Locate and identify every blood parasite.
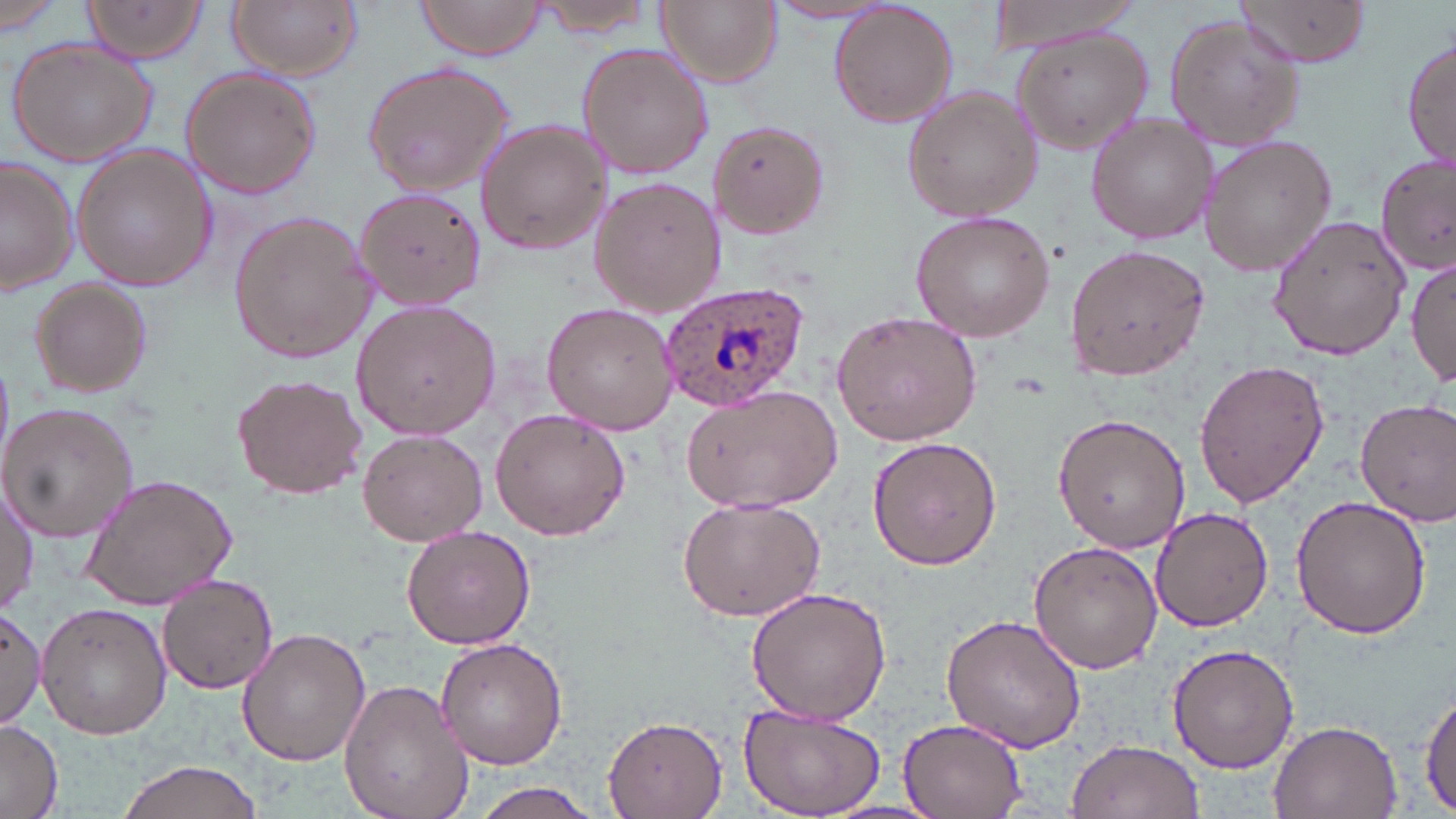

Approximate bounding boxes as [x1, y1, x2, y2] in pixels.
Plasmodium ovale-infected red blood cells: [657, 282, 811, 409].
No Plasmodium falciparum, Plasmodium malariae, Plasmodium vivax, Babesia divergens, or Trypanosoma brucei observed.

slide-level diagnosis = Plasmodium ovale
magnification = 1000x
field of view = one of a larger specimen
stain = May-Grünwald-Giemsa
preparation = thin blood smear
uninfected red blood cell locations = approximate bounding boxes as [x1, y1, x2, y2] in pixels: [80, 0, 211, 65], [226, 0, 362, 80], [529, 0, 659, 39], [658, 0, 781, 88], [985, 0, 1154, 54], [1232, 0, 1374, 70], [0, 1, 70, 33], [413, 1, 549, 63], [828, 1, 960, 130], [766, 3, 900, 25], [1162, 14, 1306, 152], [1010, 28, 1156, 155], [1401, 32, 1454, 172], [7, 37, 158, 168], [577, 42, 712, 180], [359, 59, 519, 195], [178, 66, 321, 199], [901, 85, 1041, 224], [1085, 111, 1218, 245], [707, 116, 829, 240], [472, 119, 610, 252], [1196, 133, 1336, 278], [71, 146, 217, 292], [1377, 151, 1454, 276], [0, 158, 76, 295], [588, 177, 728, 317], [354, 185, 487, 310], [227, 210, 377, 362], [908, 210, 1056, 341], [1268, 212, 1412, 360], [1063, 244, 1212, 381], [1409, 256, 1456, 387], [28, 279, 154, 400], [350, 299, 500, 438], [542, 302, 677, 434], [830, 311, 982, 446], [1193, 357, 1329, 509], [232, 373, 367, 500], [677, 383, 844, 514], [1355, 396, 1456, 528], [0, 402, 138, 541], [489, 407, 631, 541], [1052, 413, 1189, 552], [357, 428, 488, 545], [867, 436, 1001, 572], [76, 474, 239, 610], [0, 482, 38, 613], [1290, 493, 1431, 639], [676, 494, 827, 622], [1150, 505, 1276, 631], [400, 524, 535, 649], [1029, 540, 1164, 675], [157, 574, 280, 694], [741, 586, 892, 725], [36, 602, 171, 739], [1, 605, 48, 731], [939, 614, 1087, 753], [235, 626, 371, 766], [436, 637, 567, 770], [1165, 642, 1300, 773], [339, 677, 476, 819], [1416, 689, 1455, 815], [734, 703, 885, 819], [898, 716, 1029, 819], [0, 717, 62, 819], [603, 717, 727, 817], [1268, 718, 1403, 819], [1066, 738, 1203, 819], [114, 758, 269, 819], [466, 783, 607, 818]
modality = optical microscopy
image size = 1456×819 pixels